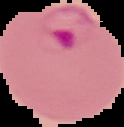

Summary:
  - Malaria status: parasitized
  - Image size: 124×127 pixels
  - Preparation: thin blood film
  - Image type: cell region segmented out of the field of view; surrounding area masked to black